Report the malaria status of this cell.
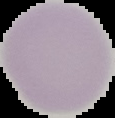
Uninfected.

preparation: thin blood smear
image_size: 115×118 pixels
image_type: segmented cell region with the area outside set to black